Give the preparation type.
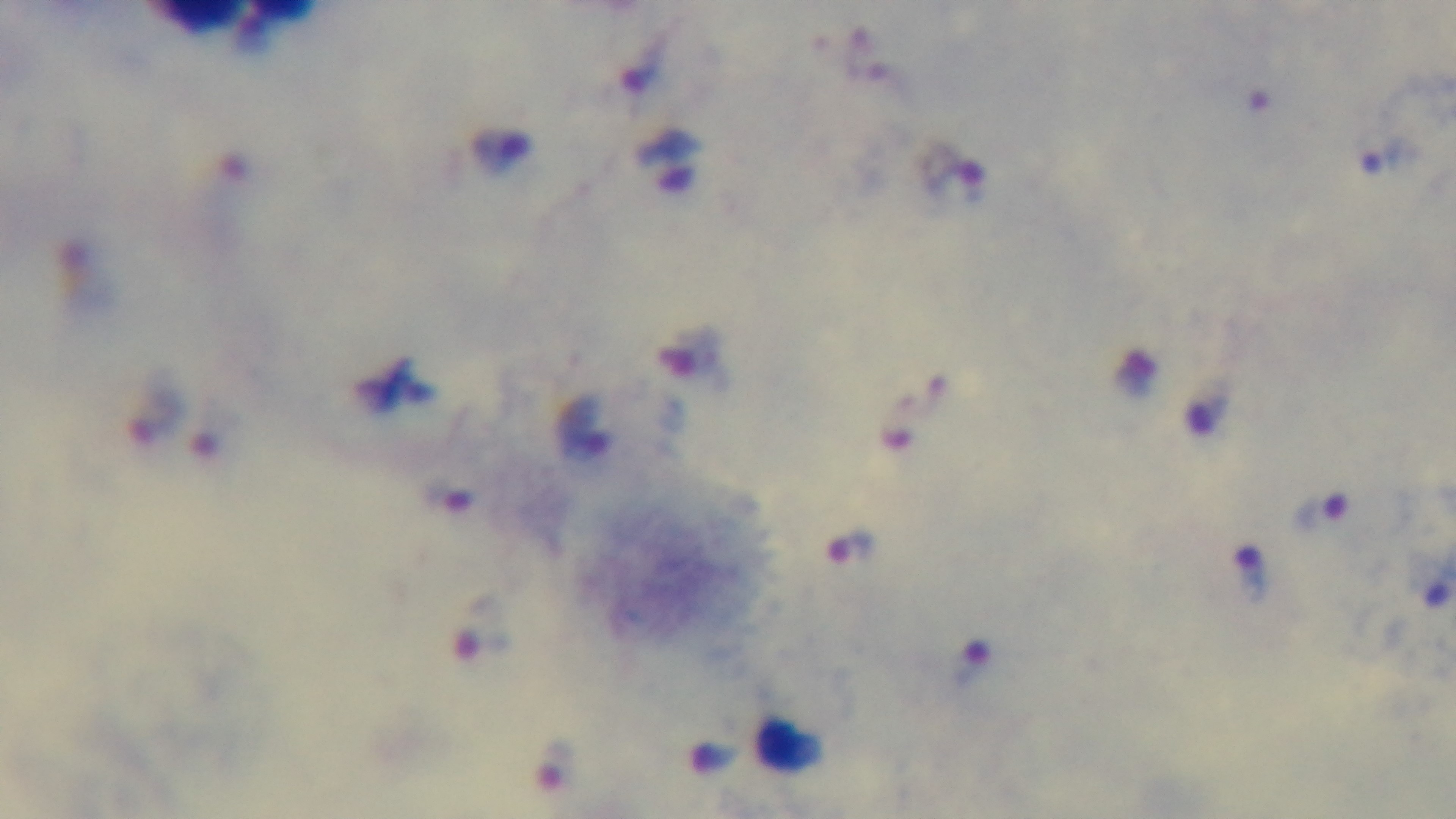

Thick.

Summary:
  - Capture: mounted 4K digital camera
  - Objective: 100x oil immersion
  - Modality: light microscopy
  - Field of view: one from the slide
  - Malaria status: positive
  - Stain: Giemsa